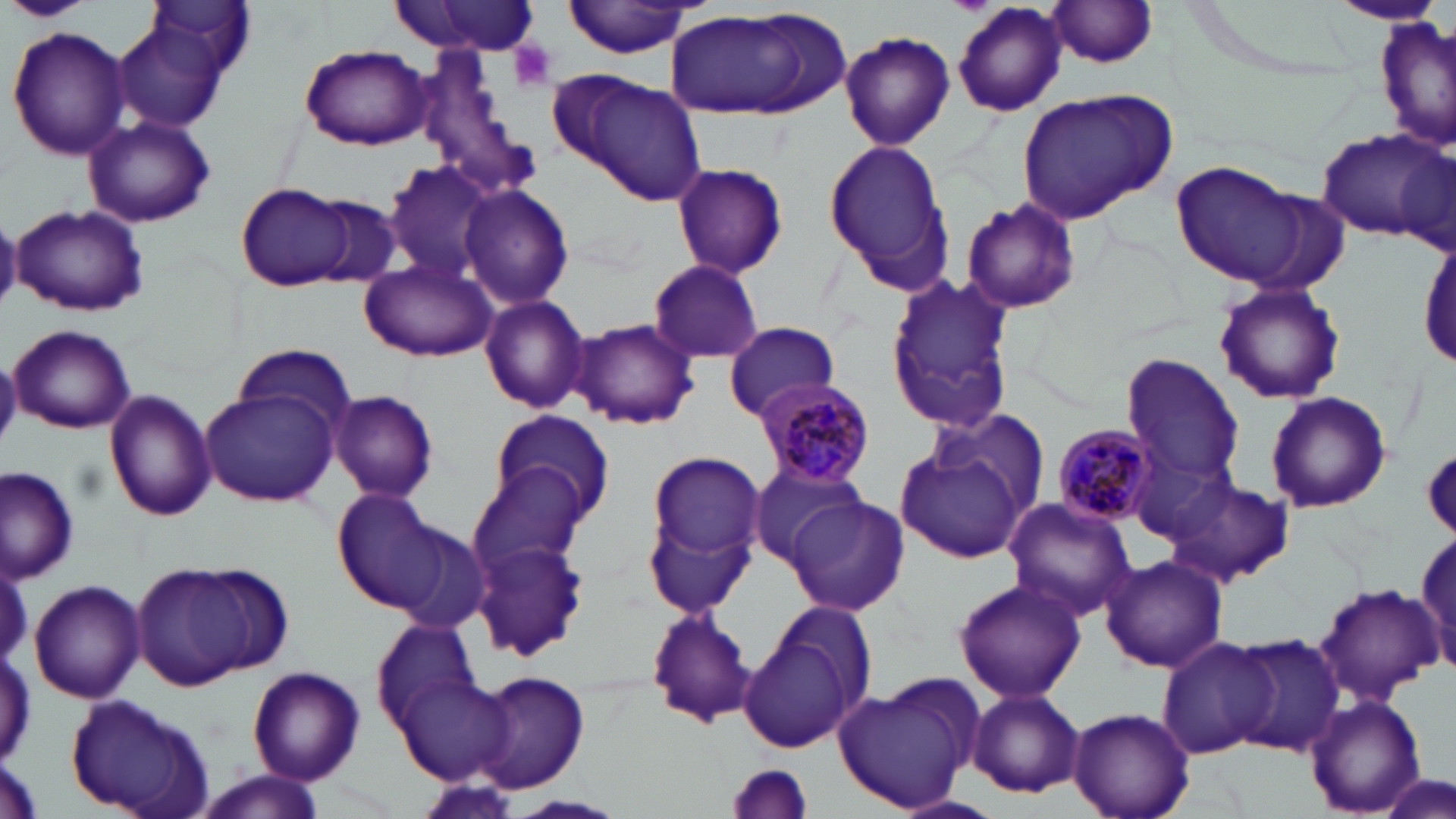

slide_level_diagnosis: Plasmodium malariae
uninfected_red_blood_cell_locations: 'approximate bounding boxes as named x1/y1/x2/y2 corners in pixels: (x1=0, y1=0, x2=92, y2=22), (x1=560, y1=0, x2=698, y2=59), (x1=148, y1=1, x2=257, y2=80), (x1=389, y1=1, x2=542, y2=57), (x1=1044, y1=1, x2=1161, y2=70), (x1=1329, y1=1, x2=1446, y2=28), (x1=951, y1=2, x2=1066, y2=116), (x1=660, y1=6, x2=847, y2=122), (x1=1375, y1=18, x2=1453, y2=155), (x1=114, y1=23, x2=226, y2=133), (x1=7, y1=25, x2=131, y2=160), (x1=840, y1=30, x2=955, y2=150), (x1=300, y1=43, x2=433, y2=151), (x1=555, y1=68, x2=706, y2=206), (x1=1016, y1=86, x2=1177, y2=223), (x1=83, y1=115, x2=216, y2=228), (x1=1313, y1=129, x2=1450, y2=239), (x1=823, y1=137, x2=954, y2=295), (x1=383, y1=160, x2=502, y2=280), (x1=1171, y1=160, x2=1311, y2=286), (x1=670, y1=161, x2=788, y2=279), (x1=234, y1=181, x2=361, y2=291), (x1=459, y1=185, x2=573, y2=311), (x1=306, y1=194, x2=406, y2=289), (x1=961, y1=197, x2=1082, y2=316), (x1=11, y1=203, x2=149, y2=317), (x1=0, y1=215, x2=21, y2=311), (x1=1418, y1=236, x2=1456, y2=369), (x1=362, y1=258, x2=496, y2=362), (x1=647, y1=259, x2=766, y2=365), (x1=883, y1=273, x2=1018, y2=437), (x1=1212, y1=281, x2=1346, y2=406), (x1=480, y1=295, x2=591, y2=413), (x1=573, y1=319, x2=699, y2=430), (x1=723, y1=321, x2=841, y2=420), (x1=9, y1=324, x2=136, y2=433), (x1=231, y1=343, x2=358, y2=436), (x1=0, y1=355, x2=21, y2=449), (x1=1121, y1=356, x2=1246, y2=484), (x1=198, y1=388, x2=337, y2=506), (x1=105, y1=389, x2=216, y2=520), (x1=331, y1=391, x2=439, y2=503), (x1=1265, y1=392, x2=1390, y2=513), (x1=922, y1=403, x2=1054, y2=529), (x1=490, y1=408, x2=614, y2=522), (x1=896, y1=433, x2=1035, y2=565), (x1=1422, y1=446, x2=1456, y2=537), (x1=645, y1=449, x2=765, y2=569), (x1=746, y1=460, x2=868, y2=569), (x1=468, y1=462, x2=602, y2=573), (x1=1, y1=467, x2=80, y2=583), (x1=1165, y1=474, x2=1294, y2=587), (x1=333, y1=489, x2=453, y2=611), (x1=784, y1=497, x2=908, y2=616), (x1=1001, y1=498, x2=1138, y2=621), (x1=646, y1=508, x2=756, y2=616), (x1=387, y1=522, x2=492, y2=635), (x1=1410, y1=530, x2=1455, y2=675), (x1=473, y1=534, x2=589, y2=661), (x1=1100, y1=552, x2=1229, y2=674), (x1=130, y1=561, x2=280, y2=692), (x1=953, y1=576, x2=1086, y2=703), (x1=27, y1=578, x2=146, y2=704), (x1=1312, y1=582, x2=1444, y2=706), (x1=647, y1=606, x2=758, y2=729), (x1=373, y1=620, x2=480, y2=730), (x1=739, y1=626, x2=863, y2=754), (x1=1231, y1=633, x2=1346, y2=756), (x1=1157, y1=637, x2=1280, y2=759), (x1=247, y1=666, x2=366, y2=785), (x1=475, y1=671, x2=590, y2=793), (x1=396, y1=676, x2=515, y2=784), (x1=835, y1=681, x2=976, y2=812), (x1=963, y1=687, x2=1086, y2=799), (x1=64, y1=696, x2=217, y2=819), (x1=1305, y1=696, x2=1427, y2=815), (x1=1069, y1=706, x2=1195, y2=819), (x1=723, y1=760, x2=811, y2=819), (x1=1374, y1=770, x2=1454, y2=819), (x1=193, y1=772, x2=330, y2=816), (x1=895, y1=793, x2=1001, y2=819)'
preparation: thin blood smear
magnification: 1000x
image_size: 1456×819 pixels
field_of_view: single
stain: May-Grünwald-Giemsa
modality: optical microscopy
platelet_locations: 'approximate bounding boxes as named x1/y1/x2/y2 corners in pixels: (x1=508, y1=40, x2=557, y2=91)'
plasmodium_malariae_infected_red_blood_cell_locations: 'approximate bounding boxes as named x1/y1/x2/y2 corners in pixels: (x1=751, y1=377, x2=876, y2=488), (x1=1053, y1=424, x2=1162, y2=526)'